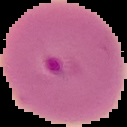

{
  "malaria_status": "parasitized",
  "image_type": "segmented cell region on a black background",
  "preparation": "thin blood film",
  "image_size": "127×127 pixels"
}